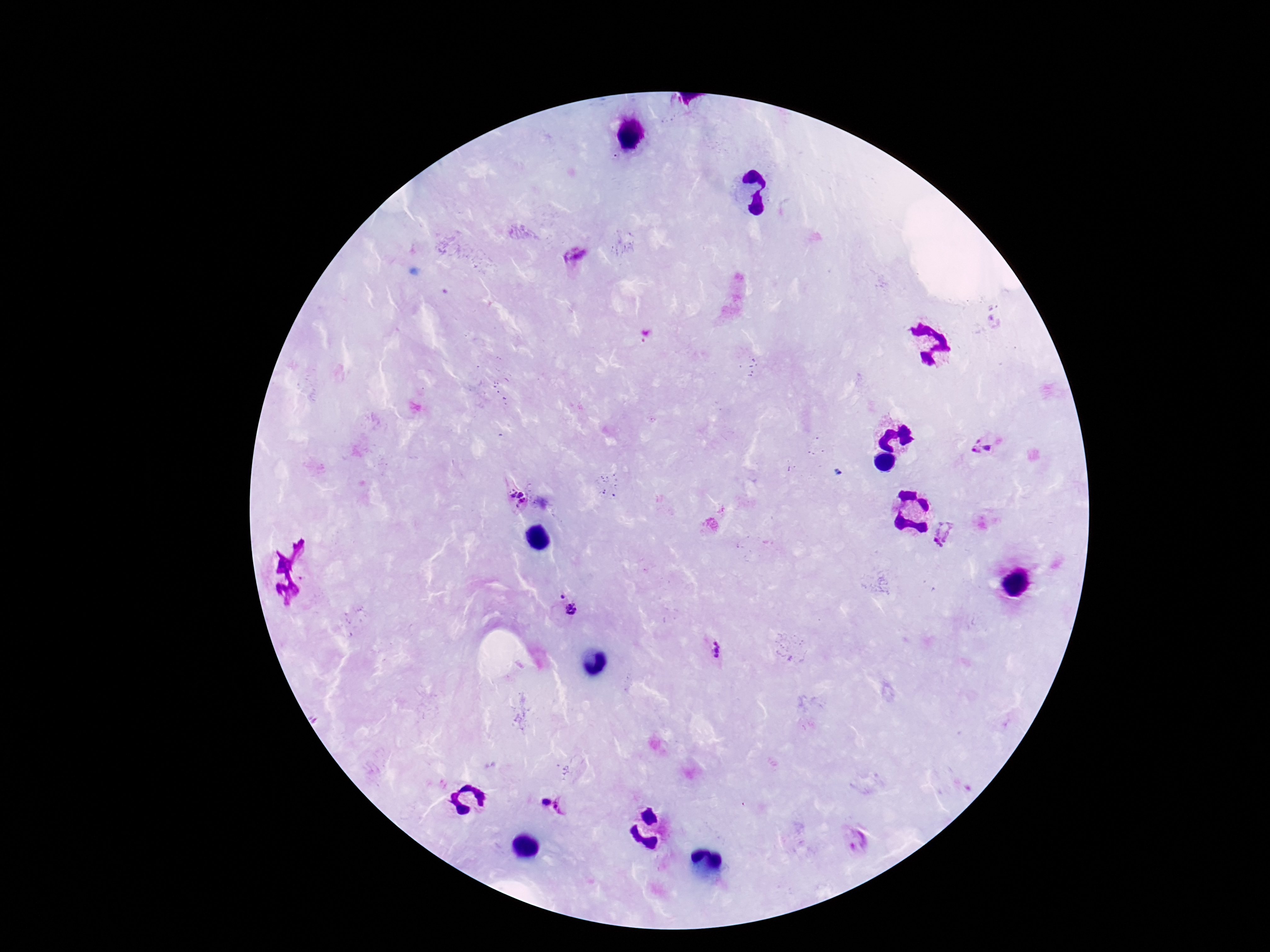 Approximate object centers, in pixels from the top-left corner. Plasmodium parasite locations: (x=575, y=253), (x=974, y=446), (x=990, y=446), (x=516, y=496), (x=948, y=538), (x=560, y=594), (x=573, y=610), (x=719, y=649), (x=545, y=802), (x=565, y=804), (x=856, y=840). Patient malaria status: positive. Thick blood film. Photographed through the microscope eyepiece with a smartphone camera. Single field of view. 100x magnification. Giemsa stain. Image is 1270×952 pixels.